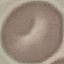

Summary:
  - Result: no malaria parasites seen
  - Capture: smartphone camera at the microscope eyepiece
  - Preparation: thin blood film
  - Image type: cell patch, automatically extracted from a larger field of view and resized to 64 × 64 pixels
  - Stain: Giemsa